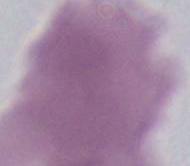
Summary:
  - Magnification: 1000x
  - Modality: photomicrograph
  - Identification: red blood cell